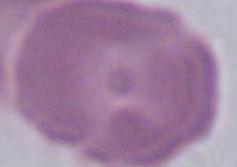
A red blood cell is shown. Captured at 1000x magnification. Photomicrograph.